Evaluate for malaria.
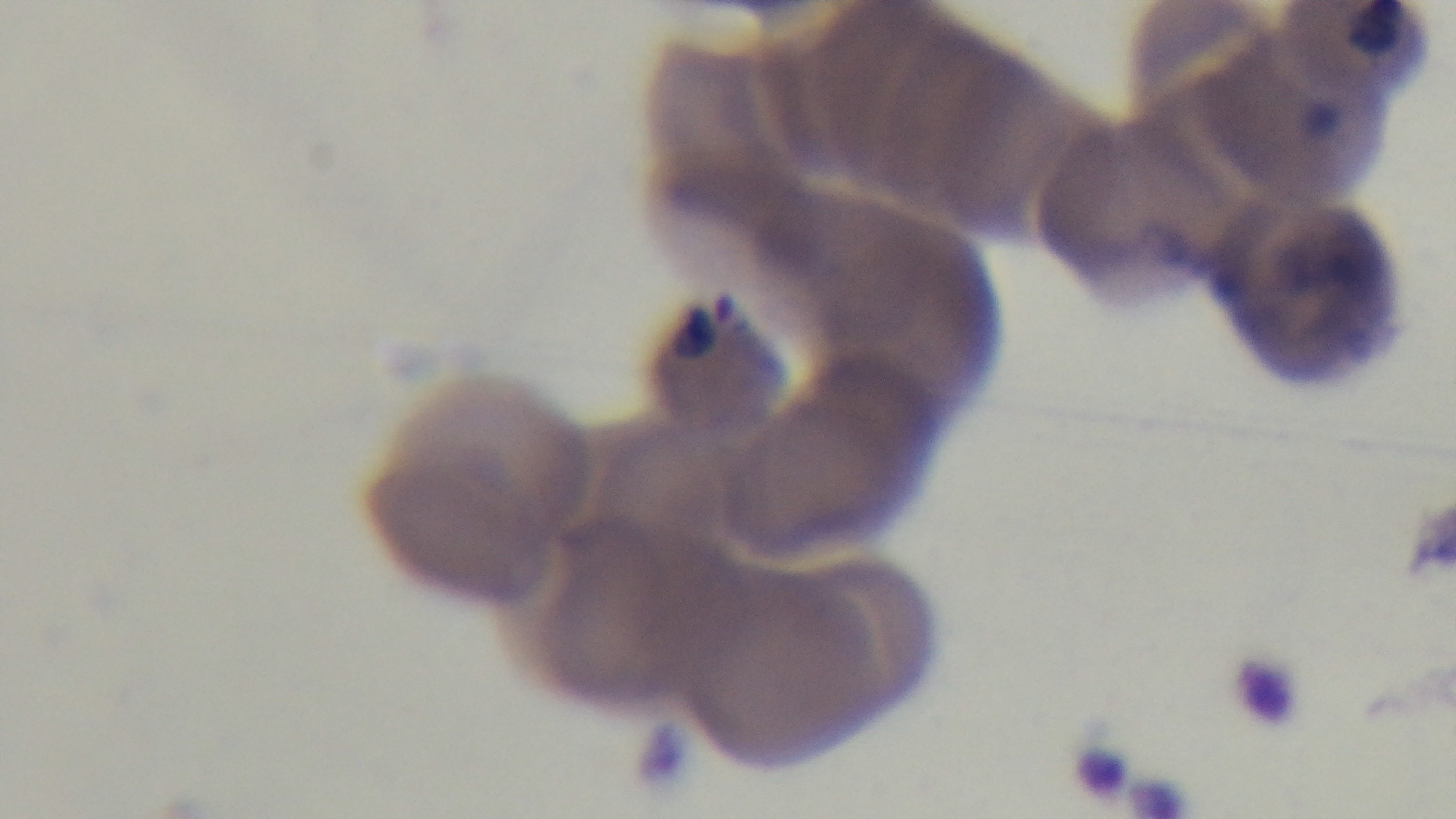

Infected.

field of view = single
modality = light microscopy
capture = mounted 4K digital camera
objective = 100x oil immersion
preparation = thin smear
stain = Giemsa